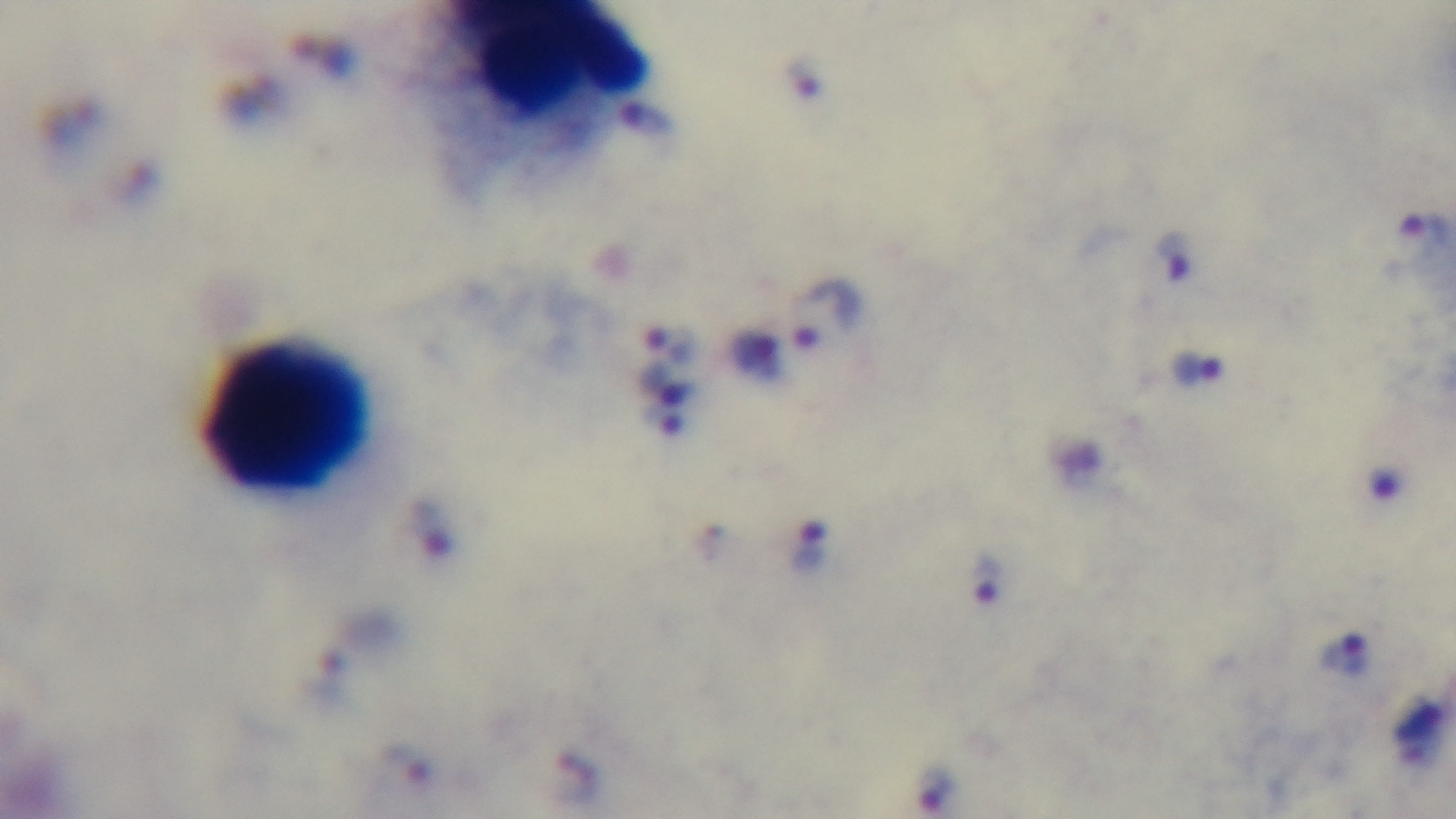
Summary:
  - Objective: 100x oil immersion
  - Field of view: single
  - Capture: mounted 4K digital camera
  - Malaria status: positive
  - Stain: Giemsa
  - Modality: light microscopy
  - Preparation: thick blood film